Name the parasite shown.
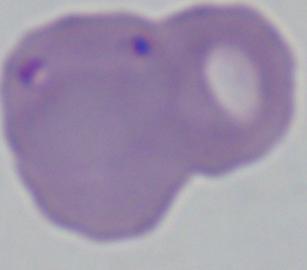
This is Babesia.

Summary:
  - Modality: photomicrograph
  - Magnification: 1000x